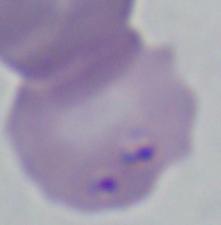
Photomicrograph. Captured at 1000x magnification. A Babesia parasite is seen.